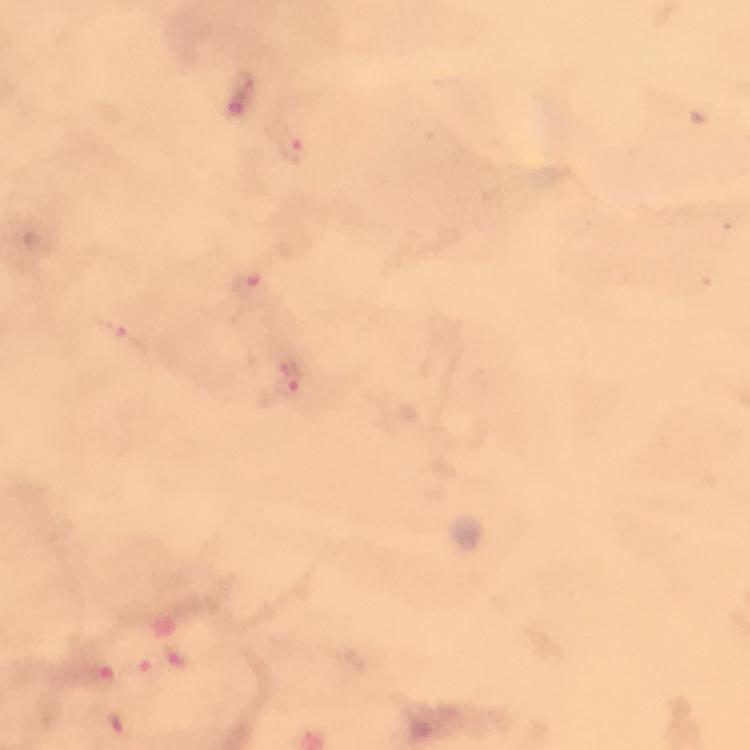

Approximate object centers, in pixels from the top-left corner.
Summary:
  - Malaria parasite locations: (x=245, y=80), (x=291, y=150), (x=244, y=285), (x=119, y=335), (x=288, y=387)
  - Image size: 750×750 pixels
  - Preparation: thick blood smear
  - Immersion oil: used
  - Context: from a diagnostic examination for malaria
  - Magnification: 100x
  - Capture: smartphone camera through the microscope
  - Cropped from: a single field of view
  - Stain: Giemsa